Locate every Plasmodium parasite.
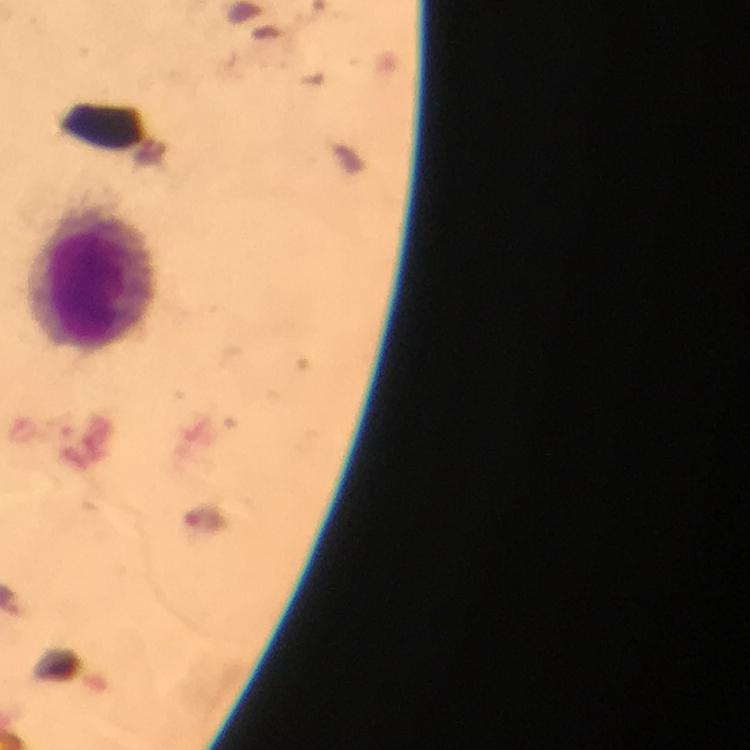
No Plasmodium parasites seen.

Approximate centers as (x, y) in pixels.
Summary:
  - Leukocyte locations: (90, 282)
  - Magnification: 100x
  - Capture: smartphone mounted on the microscope
  - Context: from a diagnostic examination for malaria
  - Preparation: thick smear
  - Stain: Giemsa
  - Cropped from: one field of view
  - Immersion oil: used
  - Image size: 750×750 pixels